Assess this cell for malaria.
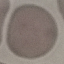
It is uninfected.

image type = cell patch, automatically extracted from a larger field of view and resized to 64 × 64 pixels
preparation = thin blood film
stain = Giemsa
capture = smartphone camera at the microscope eyepiece